Assess this cell for malaria.
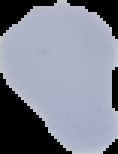

It is uninfected.

Summary:
  - Image type: segmented cell region with the area outside set to black
  - Image size: 118×154 pixels
  - Preparation: thin blood film